State the blood parasite species.
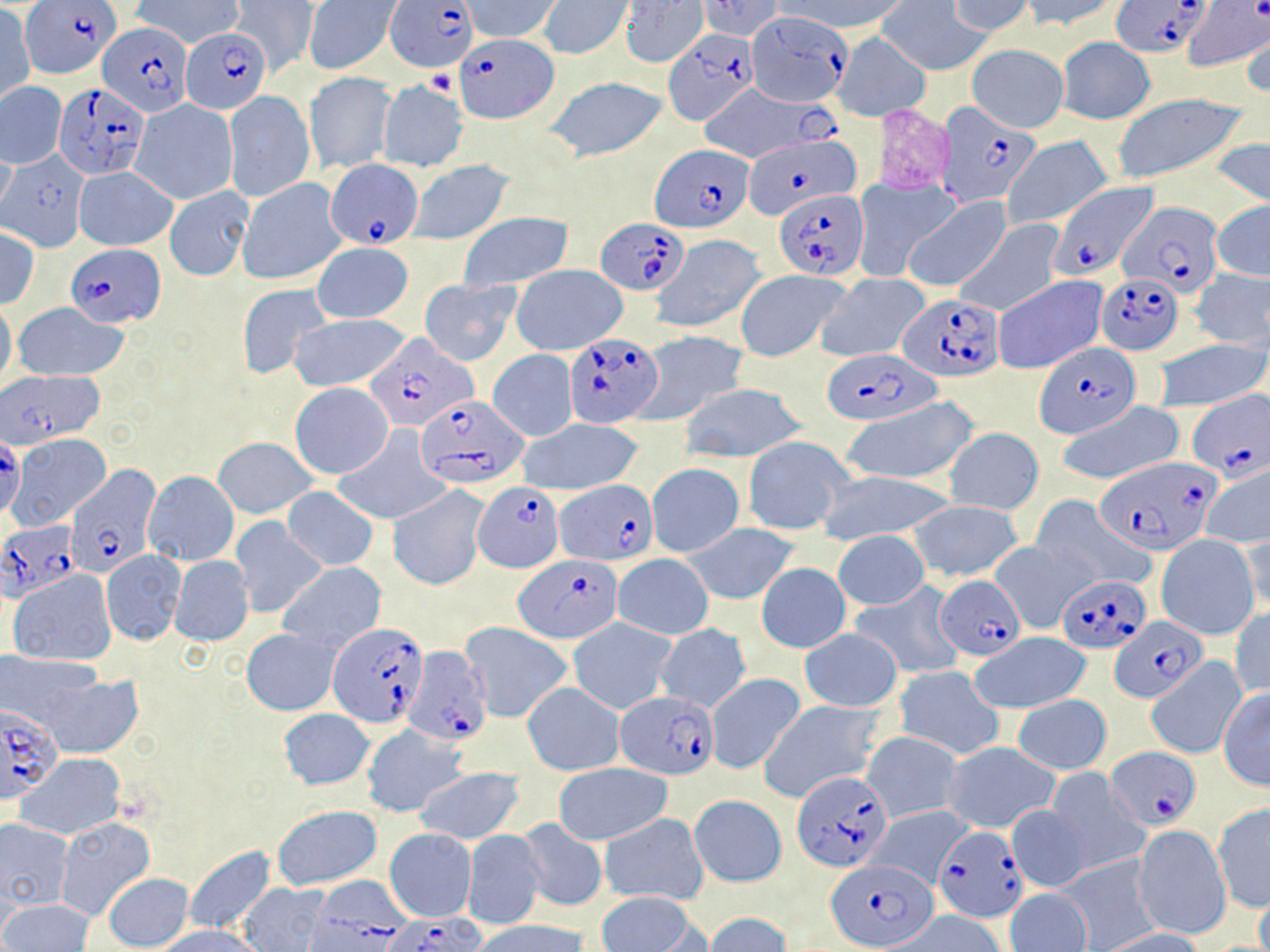
Plasmodium falciparum.

Summary:
  - Coordinate format: approximate bounding boxes as named x1/y1/x2/y2 corners in pixels
  - Plasmodium falciparum-infected red blood cell locations: (x1=386, y1=0, x2=479, y2=72), (x1=1114, y1=1, x2=1210, y2=57), (x1=1181, y1=2, x2=1270, y2=72), (x1=23, y1=3, x2=119, y2=77), (x1=746, y1=11, x2=853, y2=112), (x1=99, y1=22, x2=194, y2=118), (x1=181, y1=27, x2=271, y2=114), (x1=664, y1=30, x2=760, y2=128), (x1=454, y1=35, x2=557, y2=123), (x1=55, y1=83, x2=150, y2=179), (x1=696, y1=84, x2=844, y2=165), (x1=937, y1=102, x2=1040, y2=209), (x1=739, y1=136, x2=858, y2=218), (x1=651, y1=145, x2=755, y2=233), (x1=326, y1=158, x2=426, y2=248), (x1=1050, y1=181, x2=1159, y2=287), (x1=773, y1=188, x2=869, y2=279), (x1=1122, y1=200, x2=1223, y2=298), (x1=598, y1=217, x2=688, y2=294), (x1=67, y1=244, x2=167, y2=327), (x1=1095, y1=271, x2=1182, y2=355), (x1=898, y1=295, x2=1003, y2=380), (x1=563, y1=330, x2=664, y2=426), (x1=365, y1=333, x2=477, y2=431), (x1=1032, y1=343, x2=1141, y2=438), (x1=823, y1=349, x2=940, y2=425), (x1=0, y1=371, x2=106, y2=451), (x1=1186, y1=391, x2=1269, y2=481), (x1=416, y1=395, x2=527, y2=490), (x1=0, y1=441, x2=24, y2=511), (x1=1096, y1=456, x2=1223, y2=553), (x1=70, y1=462, x2=162, y2=572), (x1=556, y1=479, x2=656, y2=565), (x1=472, y1=482, x2=564, y2=572), (x1=0, y1=520, x2=81, y2=600), (x1=516, y1=557, x2=622, y2=643), (x1=1056, y1=573, x2=1151, y2=653), (x1=935, y1=575, x2=1026, y2=661), (x1=1111, y1=615, x2=1205, y2=704), (x1=329, y1=622, x2=428, y2=728), (x1=405, y1=645, x2=492, y2=745), (x1=616, y1=692, x2=719, y2=778), (x1=0, y1=703, x2=61, y2=803), (x1=1107, y1=745, x2=1202, y2=830), (x1=793, y1=769, x2=894, y2=873), (x1=934, y1=825, x2=1027, y2=920), (x1=828, y1=858, x2=938, y2=950), (x1=303, y1=876, x2=415, y2=952), (x1=386, y1=913, x2=487, y2=951)
  - Platelet locations: (x1=422, y1=69, x2=458, y2=97)
  - Uninfected red blood cell locations: (x1=132, y1=0, x2=244, y2=48), (x1=232, y1=0, x2=317, y2=75), (x1=302, y1=0, x2=400, y2=75), (x1=463, y1=0, x2=561, y2=44), (x1=697, y1=0, x2=783, y2=42), (x1=771, y1=0, x2=906, y2=36), (x1=1020, y1=0, x2=1125, y2=32), (x1=539, y1=1, x2=633, y2=59), (x1=620, y1=1, x2=709, y2=68), (x1=878, y1=1, x2=989, y2=75), (x1=948, y1=1, x2=1035, y2=38), (x1=0, y1=7, x2=35, y2=105), (x1=1242, y1=28, x2=1269, y2=103), (x1=832, y1=32, x2=928, y2=121), (x1=1056, y1=38, x2=1154, y2=124), (x1=967, y1=43, x2=1069, y2=133), (x1=304, y1=72, x2=395, y2=175), (x1=543, y1=76, x2=669, y2=163), (x1=378, y1=80, x2=469, y2=171), (x1=0, y1=82, x2=67, y2=168), (x1=1109, y1=90, x2=1252, y2=186), (x1=224, y1=91, x2=315, y2=202), (x1=129, y1=99, x2=239, y2=205), (x1=1001, y1=136, x2=1112, y2=231), (x1=1208, y1=136, x2=1270, y2=208), (x1=0, y1=141, x2=17, y2=218), (x1=2, y1=152, x2=91, y2=251), (x1=408, y1=160, x2=513, y2=245), (x1=75, y1=167, x2=177, y2=251), (x1=853, y1=176, x2=960, y2=281), (x1=237, y1=177, x2=347, y2=285), (x1=165, y1=185, x2=253, y2=280), (x1=902, y1=196, x2=1009, y2=294), (x1=1211, y1=201, x2=1270, y2=282), (x1=456, y1=213, x2=574, y2=292), (x1=954, y1=219, x2=1063, y2=317), (x1=0, y1=229, x2=40, y2=307), (x1=651, y1=234, x2=767, y2=334), (x1=311, y1=243, x2=414, y2=323), (x1=511, y1=264, x2=627, y2=356), (x1=1190, y1=267, x2=1270, y2=353), (x1=735, y1=269, x2=847, y2=361), (x1=818, y1=273, x2=933, y2=361), (x1=992, y1=275, x2=1106, y2=375), (x1=419, y1=277, x2=519, y2=366), (x1=237, y1=283, x2=333, y2=379), (x1=0, y1=299, x2=16, y2=390), (x1=14, y1=303, x2=129, y2=382), (x1=287, y1=312, x2=413, y2=394), (x1=635, y1=330, x2=749, y2=426), (x1=1153, y1=339, x2=1267, y2=413), (x1=487, y1=350, x2=579, y2=441), (x1=290, y1=382, x2=394, y2=479), (x1=680, y1=383, x2=807, y2=462), (x1=843, y1=400, x2=978, y2=487), (x1=1054, y1=401, x2=1185, y2=488), (x1=518, y1=418, x2=644, y2=496), (x1=333, y1=426, x2=449, y2=526), (x1=943, y1=427, x2=1045, y2=515), (x1=8, y1=432, x2=112, y2=532), (x1=214, y1=437, x2=318, y2=518), (x1=741, y1=439, x2=855, y2=536), (x1=647, y1=463, x2=745, y2=556), (x1=1201, y1=463, x2=1270, y2=550), (x1=142, y1=470, x2=239, y2=566), (x1=816, y1=471, x2=957, y2=544), (x1=283, y1=486, x2=378, y2=570), (x1=388, y1=486, x2=490, y2=590), (x1=1032, y1=496, x2=1150, y2=589), (x1=908, y1=499, x2=1023, y2=582), (x1=229, y1=517, x2=326, y2=618), (x1=685, y1=523, x2=799, y2=605), (x1=1239, y1=527, x2=1270, y2=616), (x1=834, y1=531, x2=929, y2=609), (x1=1156, y1=534, x2=1259, y2=639), (x1=990, y1=541, x2=1091, y2=632), (x1=101, y1=550, x2=185, y2=645), (x1=613, y1=554, x2=712, y2=640), (x1=170, y1=556, x2=254, y2=646), (x1=279, y1=562, x2=387, y2=651), (x1=757, y1=563, x2=851, y2=652), (x1=8, y1=570, x2=117, y2=665), (x1=853, y1=582, x2=967, y2=679), (x1=1229, y1=606, x2=1270, y2=700), (x1=568, y1=617, x2=677, y2=714), (x1=461, y1=623, x2=574, y2=723), (x1=654, y1=623, x2=752, y2=714), (x1=242, y1=628, x2=338, y2=715), (x1=799, y1=628, x2=904, y2=712), (x1=969, y1=633, x2=1091, y2=713), (x1=0, y1=653, x2=103, y2=732), (x1=1146, y1=658, x2=1246, y2=758), (x1=894, y1=666, x2=1005, y2=760), (x1=31, y1=671, x2=145, y2=758), (x1=704, y1=672, x2=805, y2=774), (x1=523, y1=683, x2=624, y2=775), (x1=1218, y1=687, x2=1270, y2=790), (x1=1013, y1=693, x2=1112, y2=774), (x1=755, y1=698, x2=885, y2=803), (x1=279, y1=709, x2=376, y2=791), (x1=359, y1=724, x2=467, y2=817), (x1=862, y1=731, x2=963, y2=823), (x1=943, y1=742, x2=1061, y2=834), (x1=17, y1=753, x2=126, y2=840), (x1=553, y1=763, x2=672, y2=845), (x1=414, y1=766, x2=524, y2=844), (x1=1045, y1=769, x2=1145, y2=874), (x1=690, y1=795, x2=786, y2=888), (x1=1212, y1=803, x2=1270, y2=913), (x1=272, y1=804, x2=382, y2=891), (x1=1007, y1=804, x2=1091, y2=892), (x1=862, y1=805, x2=972, y2=888), (x1=600, y1=813, x2=709, y2=904), (x1=0, y1=817, x2=73, y2=911), (x1=518, y1=818, x2=608, y2=912), (x1=56, y1=820, x2=155, y2=921), (x1=384, y1=828, x2=476, y2=922), (x1=1132, y1=828, x2=1232, y2=939), (x1=461, y1=830, x2=546, y2=929), (x1=183, y1=845, x2=276, y2=934), (x1=1056, y1=855, x2=1160, y2=949), (x1=103, y1=873, x2=193, y2=950), (x1=234, y1=883, x2=332, y2=951), (x1=1006, y1=888, x2=1093, y2=952), (x1=1254, y1=889, x2=1270, y2=952), (x1=597, y1=891, x2=701, y2=952), (x1=1, y1=898, x2=94, y2=952), (x1=705, y1=912, x2=791, y2=952), (x1=888, y1=913, x2=1009, y2=952), (x1=472, y1=921, x2=589, y2=952), (x1=155, y1=926, x2=266, y2=952), (x1=1097, y1=928, x2=1210, y2=952)
  - Magnification: 1000x
  - Image size: 1270×952 pixels
  - Preparation: thin blood smear
  - Field of view: single
  - Modality: optical microscopy
  - Stain: May-Grünwald-Giemsa